Give the position of every Plasmodium parasite visible.
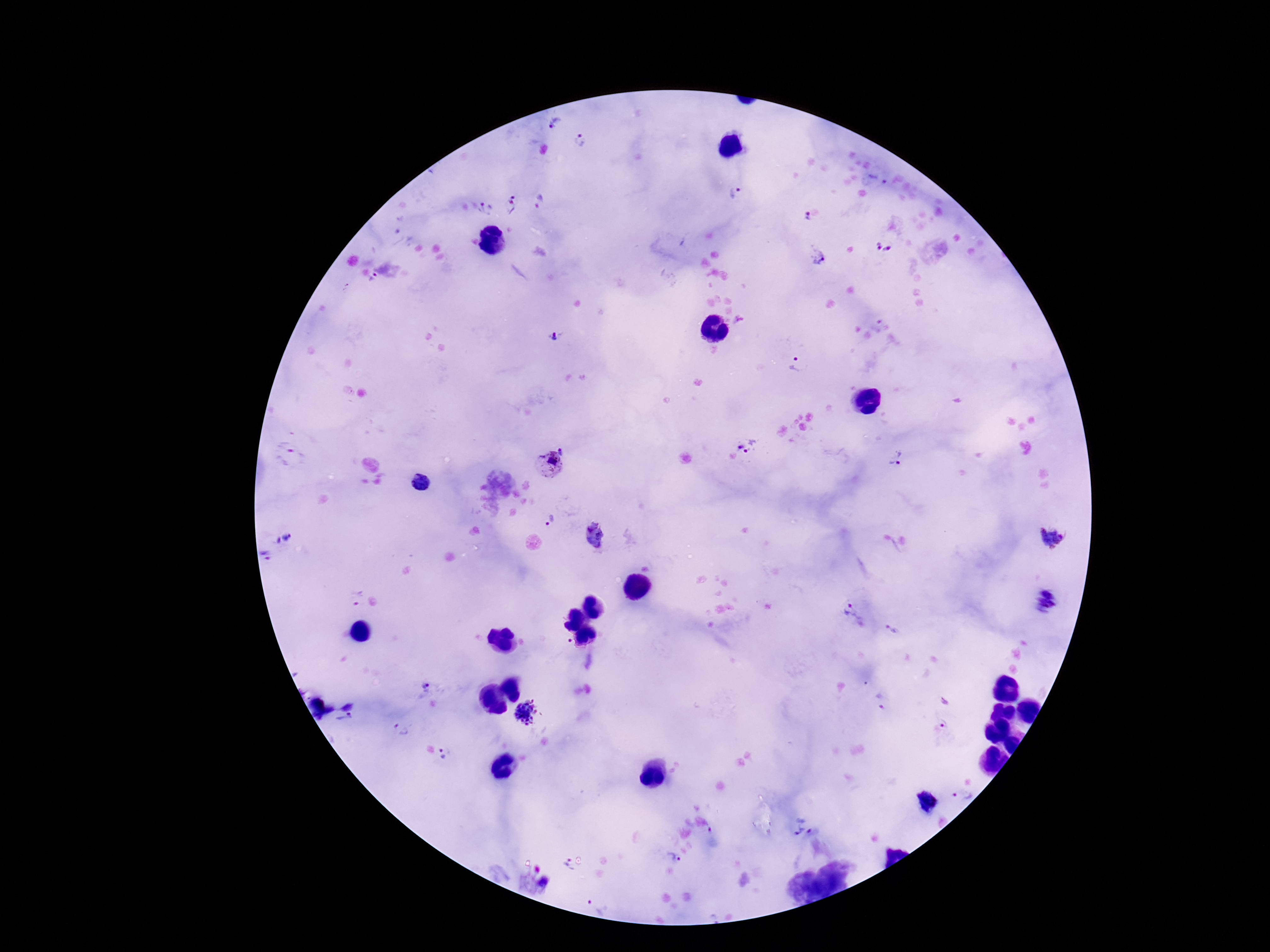

Approximate centers as [x, y] in pixels.
Plasmodium parasites: [557, 123], [580, 140], [736, 192], [513, 196], [488, 209], [806, 218], [884, 247], [817, 257], [375, 275], [346, 286], [556, 337], [795, 364], [748, 446], [563, 450], [289, 456], [897, 459], [548, 465], [421, 483], [549, 521], [593, 536], [287, 537], [1050, 538], [267, 555], [354, 599], [1044, 601], [856, 615], [892, 629], [424, 687], [945, 700], [881, 707], [527, 711], [347, 722], [945, 724], [399, 730], [444, 755], [962, 797], [802, 826], [712, 830], [674, 857], [566, 866], [543, 883], [598, 904].

Giemsa-stained preparation. Single field of view. 100x magnification. Patient malaria status: positive. Smartphone photograph taken through the microscope eyepiece. Image is 1270×952 pixels. Thick blood smear.